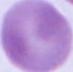
Summary:
  - Identification: red blood cell
  - Modality: photomicrograph
  - Magnification: 1000x